Name the parasite shown.
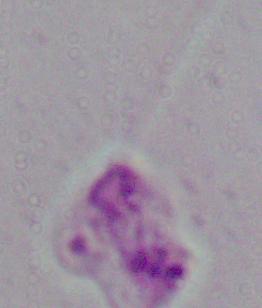
Leishmania.

Summary:
  - Modality: photomicrograph
  - Magnification: 1000x